Name the blood parasite species.
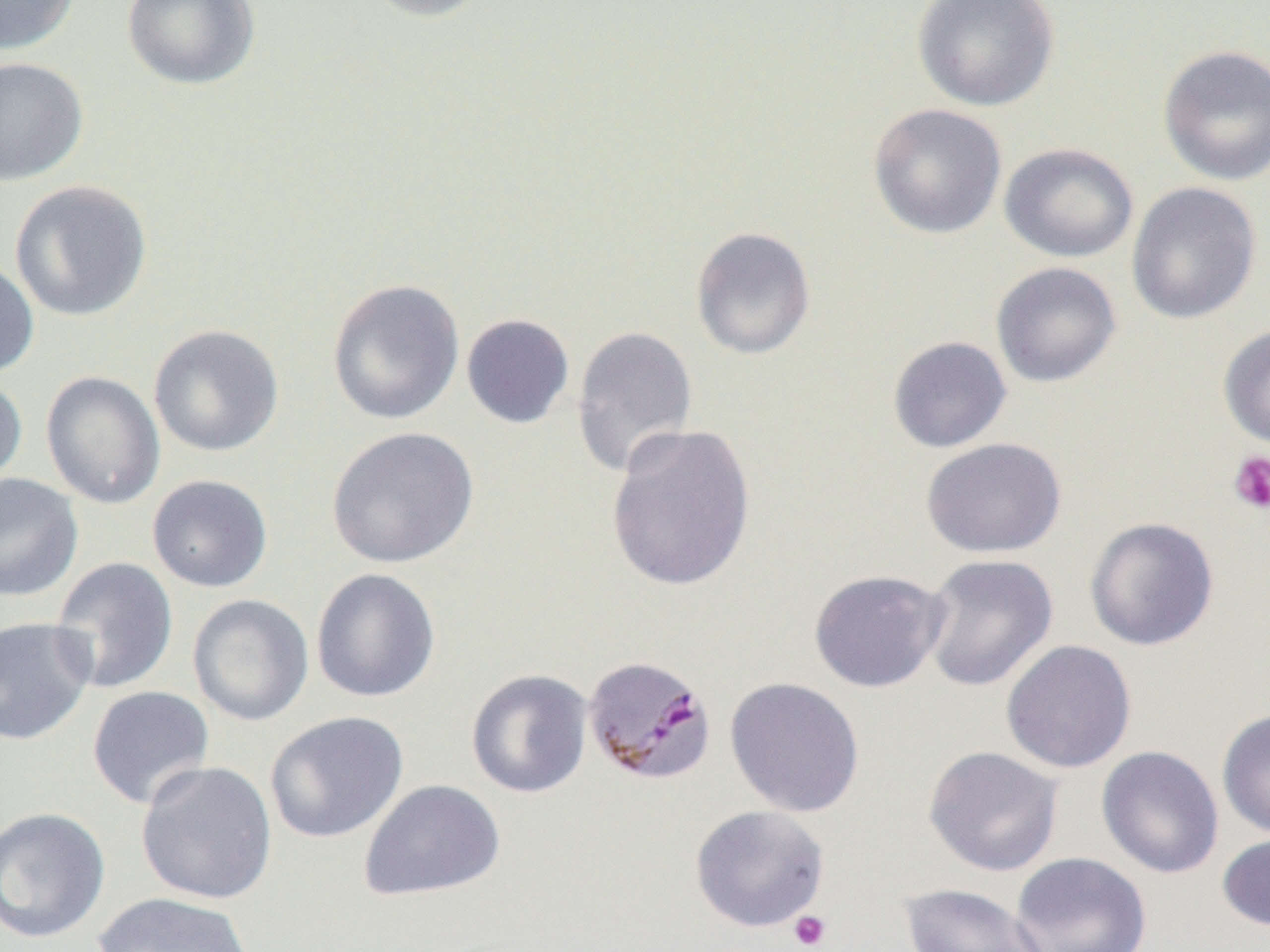
Plasmodium malariae.

field of view = single
preparation = thin blood smear
platelet locations = approximate bounding boxes as named x1/y1/x2/y2 corners in pixels: (x1=1228, y1=451, x2=1270, y2=515), (x1=788, y1=910, x2=832, y2=950)
Plasmodium malariae-infected red blood cell locations = approximate bounding boxes as named x1/y1/x2/y2 corners in pixels: (x1=583, y1=655, x2=716, y2=784)
modality = light microscopy
uninfected red blood cell locations = approximate bounding boxes as named x1/y1/x2/y2 corners in pixels: (x1=0, y1=0, x2=80, y2=55), (x1=121, y1=0, x2=261, y2=91), (x1=357, y1=0, x2=495, y2=22), (x1=912, y1=1, x2=1061, y2=111), (x1=1157, y1=44, x2=1270, y2=186), (x1=0, y1=56, x2=89, y2=186), (x1=867, y1=103, x2=1007, y2=240), (x1=999, y1=142, x2=1139, y2=263), (x1=9, y1=179, x2=153, y2=322), (x1=1126, y1=181, x2=1262, y2=325), (x1=690, y1=225, x2=817, y2=360), (x1=0, y1=257, x2=40, y2=379), (x1=990, y1=261, x2=1122, y2=388), (x1=326, y1=278, x2=465, y2=425), (x1=461, y1=313, x2=575, y2=429), (x1=1218, y1=323, x2=1270, y2=449), (x1=148, y1=324, x2=285, y2=457), (x1=571, y1=325, x2=698, y2=478), (x1=887, y1=336, x2=1012, y2=453), (x1=40, y1=370, x2=165, y2=510), (x1=0, y1=372, x2=28, y2=491), (x1=605, y1=422, x2=757, y2=593), (x1=326, y1=426, x2=479, y2=569), (x1=920, y1=437, x2=1067, y2=558), (x1=0, y1=473, x2=83, y2=601), (x1=147, y1=474, x2=273, y2=593), (x1=1084, y1=517, x2=1220, y2=651), (x1=920, y1=554, x2=1058, y2=692), (x1=50, y1=557, x2=179, y2=694), (x1=311, y1=568, x2=441, y2=703), (x1=808, y1=569, x2=949, y2=693), (x1=187, y1=593, x2=314, y2=726), (x1=0, y1=616, x2=96, y2=745), (x1=1000, y1=640, x2=1137, y2=773), (x1=465, y1=668, x2=593, y2=798), (x1=725, y1=677, x2=865, y2=817), (x1=86, y1=685, x2=215, y2=810), (x1=1216, y1=709, x2=1270, y2=839), (x1=264, y1=710, x2=409, y2=844), (x1=1096, y1=745, x2=1225, y2=879), (x1=923, y1=746, x2=1064, y2=877), (x1=135, y1=760, x2=278, y2=905), (x1=358, y1=779, x2=506, y2=902), (x1=689, y1=804, x2=830, y2=932), (x1=0, y1=806, x2=111, y2=944), (x1=1217, y1=831, x2=1270, y2=933), (x1=1010, y1=852, x2=1153, y2=952), (x1=899, y1=882, x2=1051, y2=952), (x1=92, y1=892, x2=255, y2=952)
image size = 1270×952 pixels
magnification = 1000x